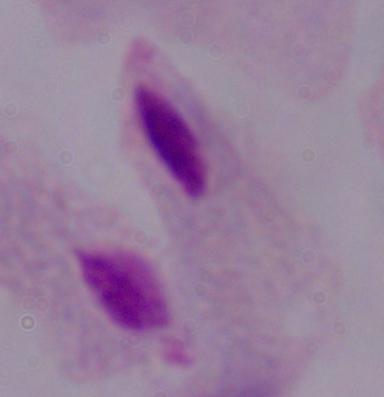
A trichomonad is seen. 1000x magnification. Micrograph.